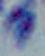

Summary:
  - Magnification: 1000x
  - Identification: Toxoplasma gondii
  - Modality: micrograph